Assess the morphology of the erythrocytes.
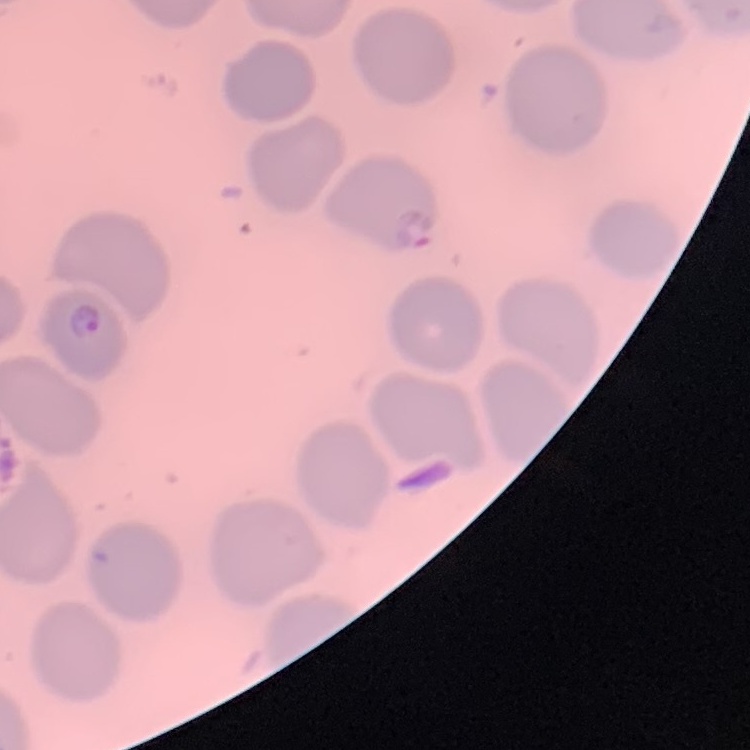

No rouleaux formation.

Thin blood film. One tile cut from a larger photomicrograph. Field's or Giemsa stain.